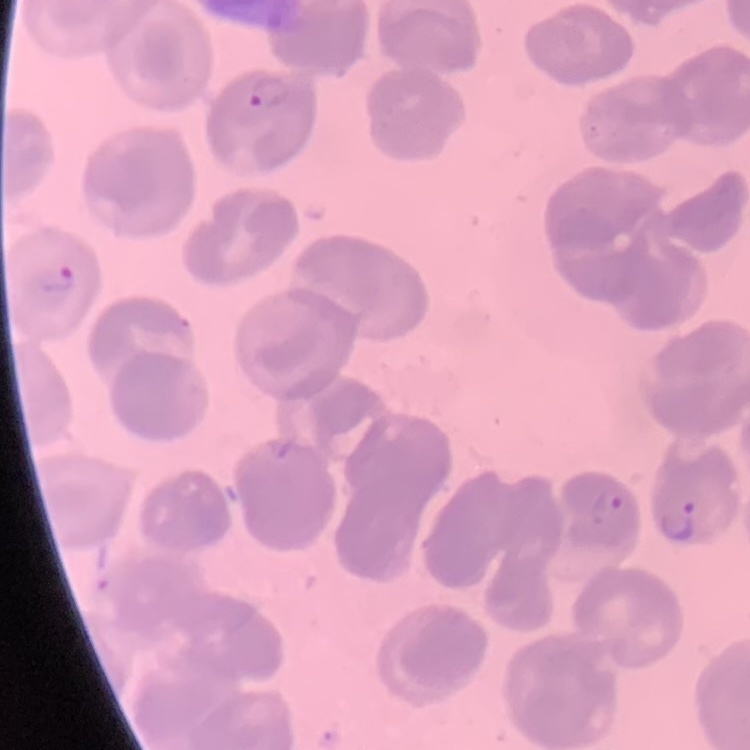

Summary:
  - Erythrocyte morphology: no rouleaux formation
  - Stain: Field's or Giemsa
  - Image type: square crop of a larger photomicrograph
  - Preparation: thin blood film